Give the position of every Plasmodium parasite visible.
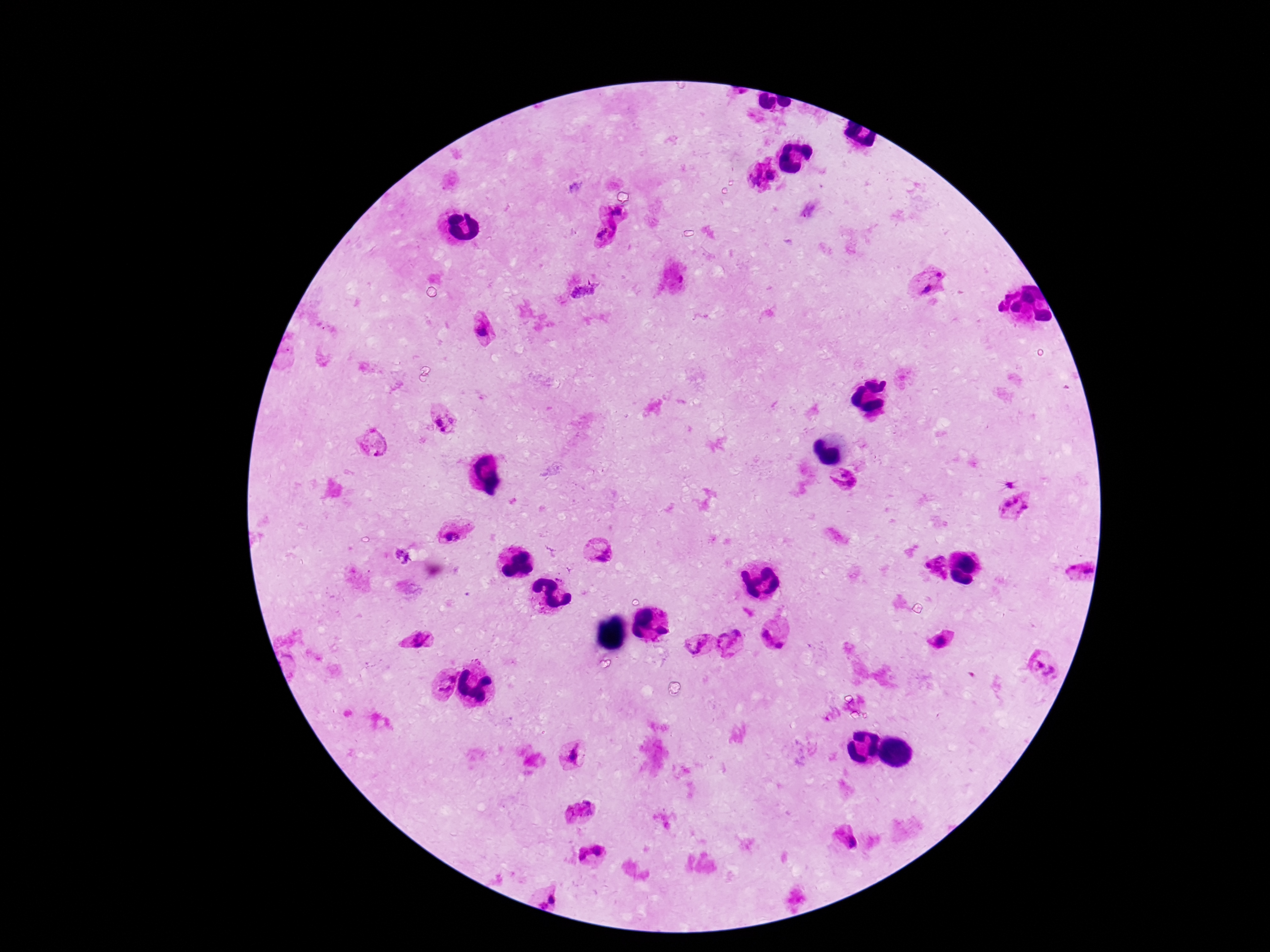
Approximate object centers, in pixels from the top-left corner.
Plasmodium parasites: (x=771, y=175), (x=754, y=178), (x=615, y=212), (x=605, y=233), (x=938, y=274), (x=927, y=290), (x=483, y=332), (x=438, y=421), (x=444, y=431), (x=376, y=443), (x=1016, y=499), (x=1007, y=506), (x=1026, y=507), (x=449, y=536), (x=599, y=551), (x=403, y=557), (x=936, y=566), (x=1071, y=568), (x=1088, y=570), (x=766, y=635), (x=416, y=639), (x=733, y=640), (x=940, y=642), (x=699, y=645), (x=779, y=645), (x=1045, y=668), (x=443, y=684), (x=572, y=756), (x=581, y=810), (x=845, y=837), (x=589, y=857), (x=554, y=898), (x=544, y=904).

stain = Giemsa
image size = 1270×952 pixels
field of view = single
preparation = thick peripheral-blood smear
patient malaria status = infected
magnification = 100x
capture = smartphone camera through the microscope eyepiece